Assess this cell for malaria.
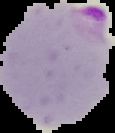
Parasitized.

Segmented cell region on a black background. Image is 115×133 pixels. From a thin blood smear.